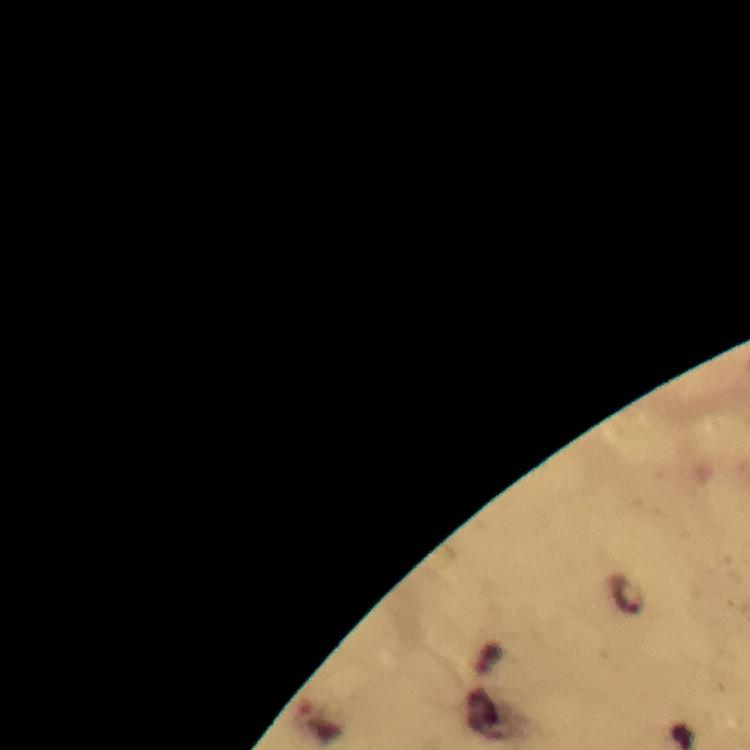

capture = smartphone photograph through a microscope
stain = Giemsa
image size = 750×750 pixels
magnification = 100x
Plasmodium parasite locations = approximate object centers, in pixels from the top-left corner: (x=626, y=594)
preparation = thick blood film
cropped from = one field of view
context = from a diagnostic examination for malaria
immersion oil = used